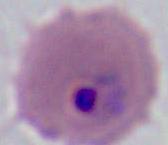

Summary:
  - Identification: Plasmodium
  - Modality: micrograph
  - Magnification: 400x or 1000x